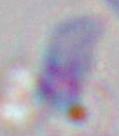
Captured at 1000x magnification. Toxoplasma gondii is shown. Photomicrograph.